Name the cell type shown.
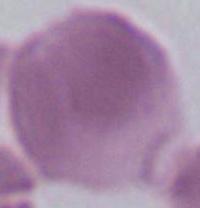
An erythrocyte.

Micrograph. 1000x magnification.